Locate and identify every blood parasite.
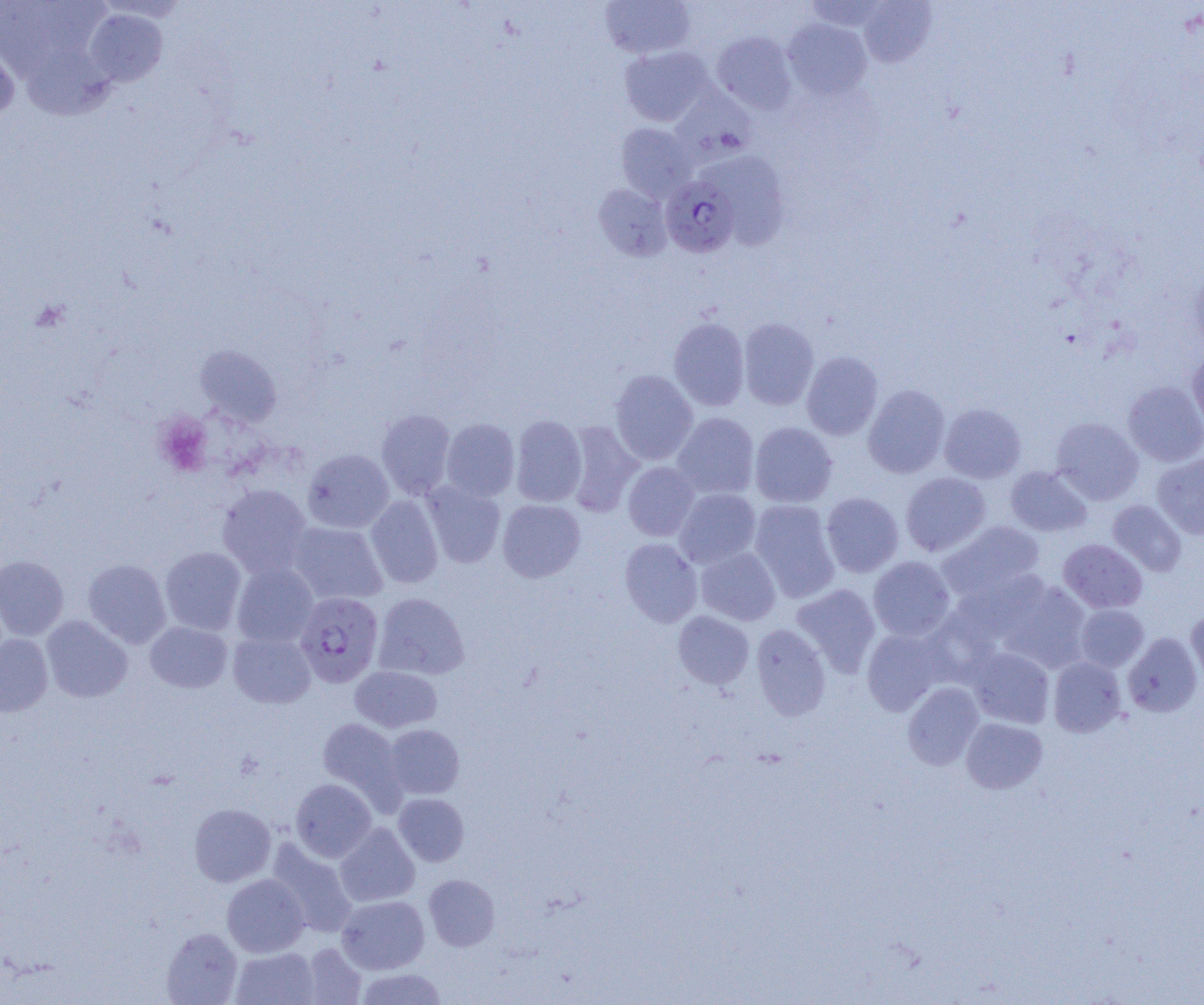
Approximate bounding boxes as named x1/y1/x2/y2 corners in pixels.
Plasmodium falciparum-infected red blood cells: (x1=660, y1=175, x2=739, y2=258), (x1=295, y1=592, x2=383, y2=687).
No Plasmodium ovale, Plasmodium malariae, Plasmodium vivax, Babesia divergens, or Trypanosoma brucei observed.

Platelet locations: (x1=154, y1=413, x2=214, y2=477). Uninfected red blood cell locations: (x1=858, y1=0, x2=937, y2=68), (x1=600, y1=1, x2=696, y2=59), (x1=83, y1=8, x2=168, y2=87), (x1=783, y1=19, x2=872, y2=100), (x1=712, y1=32, x2=798, y2=114), (x1=0, y1=38, x2=20, y2=124), (x1=15, y1=38, x2=116, y2=120), (x1=619, y1=45, x2=713, y2=126), (x1=670, y1=88, x2=757, y2=163), (x1=616, y1=122, x2=697, y2=202), (x1=710, y1=151, x2=789, y2=250), (x1=593, y1=183, x2=672, y2=261), (x1=668, y1=317, x2=750, y2=411), (x1=738, y1=318, x2=819, y2=410), (x1=195, y1=345, x2=281, y2=427), (x1=1187, y1=348, x2=1204, y2=437), (x1=801, y1=351, x2=883, y2=440), (x1=610, y1=369, x2=698, y2=465), (x1=1123, y1=381, x2=1204, y2=466), (x1=863, y1=384, x2=951, y2=478), (x1=939, y1=403, x2=1026, y2=483), (x1=376, y1=409, x2=456, y2=500), (x1=672, y1=412, x2=759, y2=499), (x1=510, y1=415, x2=587, y2=507), (x1=1050, y1=417, x2=1143, y2=505), (x1=440, y1=419, x2=519, y2=502), (x1=565, y1=421, x2=643, y2=516), (x1=750, y1=422, x2=837, y2=507), (x1=303, y1=449, x2=394, y2=533), (x1=1151, y1=453, x2=1204, y2=539), (x1=623, y1=462, x2=700, y2=541), (x1=1005, y1=466, x2=1092, y2=537), (x1=900, y1=472, x2=991, y2=556), (x1=422, y1=481, x2=506, y2=567), (x1=217, y1=484, x2=312, y2=577), (x1=674, y1=488, x2=761, y2=568), (x1=821, y1=492, x2=903, y2=577), (x1=365, y1=496, x2=444, y2=589), (x1=497, y1=499, x2=585, y2=582), (x1=749, y1=499, x2=840, y2=602), (x1=1107, y1=500, x2=1187, y2=576), (x1=287, y1=521, x2=388, y2=605), (x1=937, y1=521, x2=1045, y2=601), (x1=619, y1=538, x2=703, y2=627), (x1=1058, y1=538, x2=1147, y2=613), (x1=160, y1=546, x2=246, y2=635), (x1=696, y1=546, x2=781, y2=625), (x1=0, y1=555, x2=69, y2=640), (x1=868, y1=556, x2=955, y2=641), (x1=83, y1=559, x2=171, y2=648), (x1=231, y1=562, x2=318, y2=648), (x1=998, y1=580, x2=1091, y2=673), (x1=791, y1=584, x2=881, y2=677), (x1=373, y1=592, x2=470, y2=680), (x1=1075, y1=604, x2=1149, y2=672), (x1=1186, y1=609, x2=1204, y2=688), (x1=673, y1=611, x2=754, y2=689), (x1=41, y1=615, x2=132, y2=702), (x1=145, y1=621, x2=232, y2=693), (x1=751, y1=623, x2=831, y2=721), (x1=862, y1=627, x2=947, y2=716), (x1=228, y1=631, x2=316, y2=708), (x1=1123, y1=633, x2=1202, y2=717), (x1=0, y1=634, x2=53, y2=716), (x1=967, y1=647, x2=1055, y2=728), (x1=1048, y1=657, x2=1126, y2=737), (x1=350, y1=665, x2=443, y2=733), (x1=902, y1=682, x2=984, y2=770), (x1=961, y1=717, x2=1048, y2=793), (x1=318, y1=718, x2=404, y2=807), (x1=384, y1=724, x2=464, y2=799), (x1=290, y1=778, x2=376, y2=862), (x1=393, y1=793, x2=469, y2=866), (x1=189, y1=803, x2=276, y2=887), (x1=334, y1=823, x2=419, y2=907), (x1=266, y1=839, x2=358, y2=937), (x1=222, y1=873, x2=309, y2=957), (x1=424, y1=874, x2=500, y2=951), (x1=337, y1=894, x2=429, y2=974), (x1=161, y1=928, x2=243, y2=1004), (x1=302, y1=943, x2=367, y2=1004), (x1=231, y1=947, x2=320, y2=1005), (x1=355, y1=968, x2=447, y2=1004). Slide-level diagnosis: Plasmodium falciparum. One field of a larger specimen. Light microscopy. Thin blood smear. Captured at 1000x magnification. Image is 1204×1005 pixels.